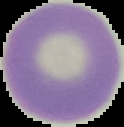

{
  "image_size": "124×127 pixels",
  "preparation": "thin blood smear",
  "result": "no malaria parasites seen",
  "image_type": "segmented cell region with the area outside set to black"
}